State which cell type is depicted.
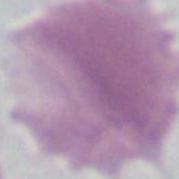

An erythrocyte.

Micrograph. 1000x magnification.